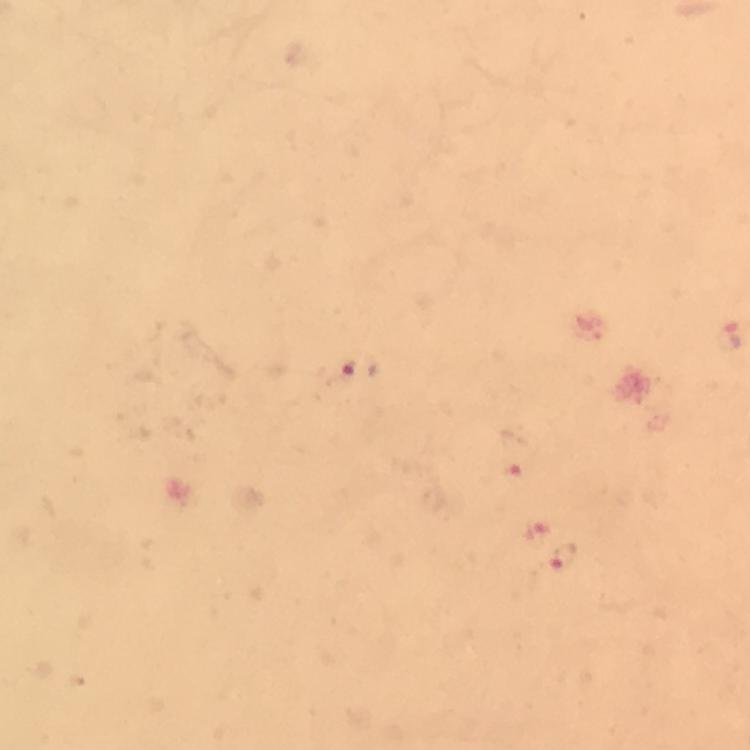

Approximate centers as [x, y] in pixels.
Summary:
  - Plasmodium parasite locations: [360, 370], [513, 453], [537, 527], [565, 557]
  - Image size: 750×750 pixels
  - Magnification: 100x
  - Stain: Giemsa
  - Immersion oil: used
  - Preparation: thick smear
  - Capture: smartphone photograph through a microscope
  - Cropped from: a single field of view
  - Context: from a malaria diagnostic workup